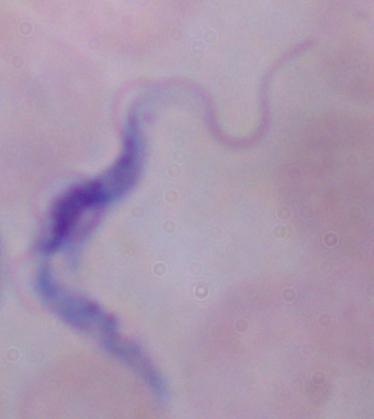

Summary:
  - Modality: photomicrograph
  - Identification: trypanosome
  - Magnification: 1000x